Name the parasite shown.
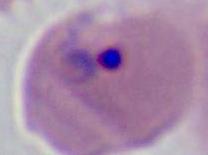

Plasmodium.

Summary:
  - Modality: photomicrograph
  - Magnification: 400x or 1000x